Assess this cell for malaria.
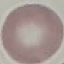

Uninfected.

{
  "preparation": "thin smear",
  "image_type": "cell patch, automatically extracted from a larger field of view and resized to 64 × 64 pixels",
  "capture": "smartphone camera at the microscope eyepiece",
  "stain": "Giemsa"
}